State which parasite is depicted.
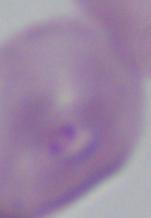
This is Babesia.

Summary:
  - Modality: micrograph
  - Magnification: 1000x